Assess this cell for malaria.
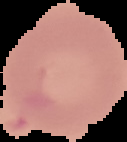
Uninfected.

{
  "image_type": "segmented cell region on a black background",
  "image_size": "127×142 pixels",
  "preparation": "thin blood film"
}